Locate and identify every blood parasite.
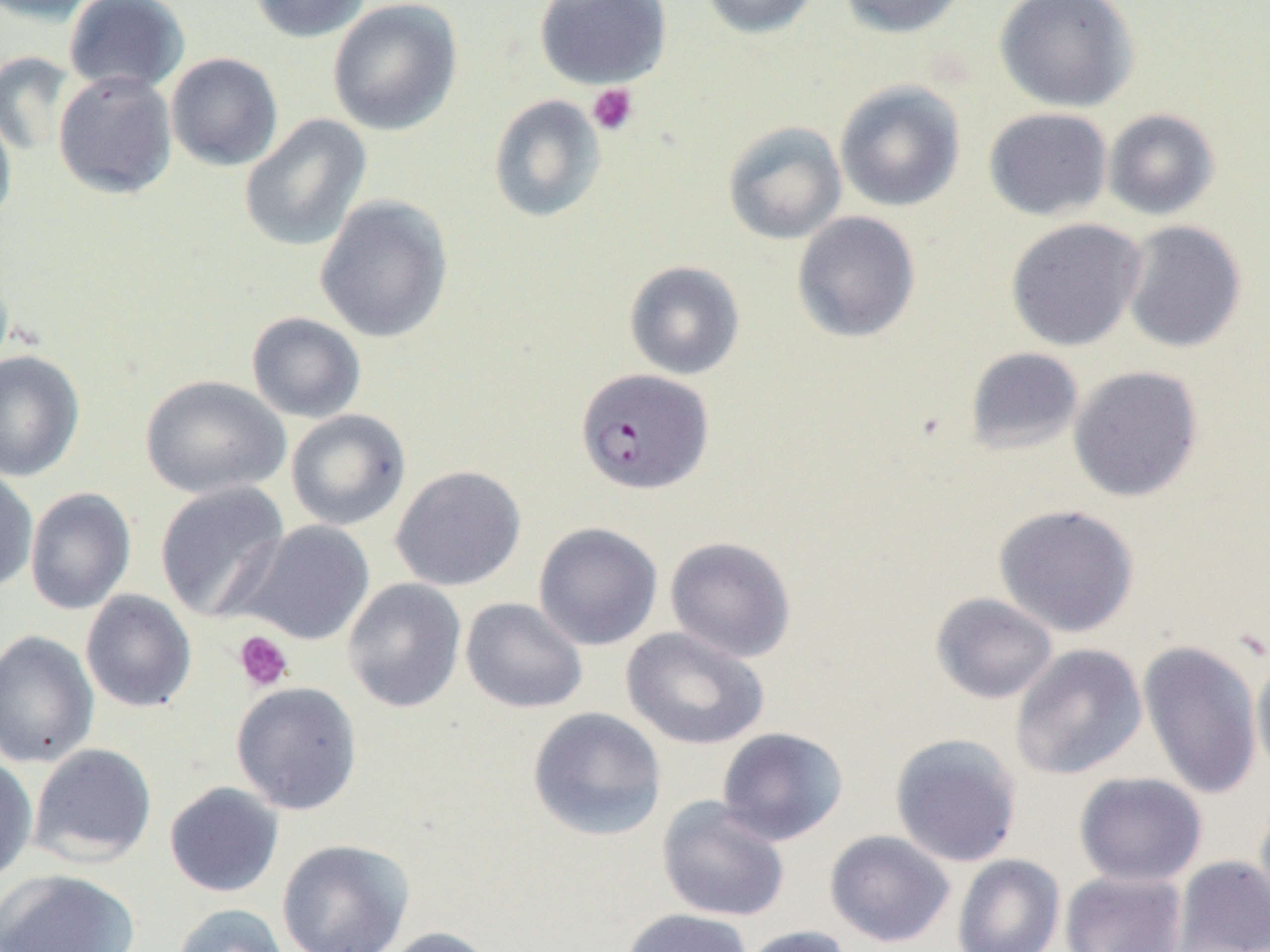

Approximate bounding boxes as [x1, y1, x2, y2] in pixels.
Plasmodium falciparum-infected red blood cells: [575, 368, 713, 495].
No Plasmodium ovale, Plasmodium malariae, Plasmodium vivax, Babesia divergens, or Trypanosoma brucei observed.

Uninfected red blood cell locations: [64, 0, 190, 94], [249, 0, 373, 43], [534, 0, 671, 89], [698, 0, 822, 39], [836, 0, 968, 38], [995, 0, 1140, 112], [0, 1, 102, 25], [327, 1, 463, 136], [0, 50, 75, 156], [166, 52, 283, 171], [53, 71, 177, 199], [834, 81, 965, 212], [488, 95, 606, 223], [0, 102, 17, 232], [983, 107, 1113, 221], [990, 108, 1116, 348], [1103, 108, 1221, 220], [239, 114, 372, 253], [722, 121, 847, 245], [314, 194, 454, 343], [792, 211, 921, 343], [1005, 218, 1145, 351], [1120, 220, 1247, 353], [624, 260, 745, 380], [246, 311, 366, 423], [965, 346, 1084, 456], [0, 350, 85, 482], [1068, 365, 1203, 502], [140, 374, 291, 499], [285, 409, 411, 531], [391, 464, 526, 592], [0, 467, 38, 593], [155, 481, 290, 622], [24, 487, 136, 615], [994, 503, 1139, 637], [237, 520, 374, 646], [533, 522, 663, 651], [665, 536, 796, 662], [342, 578, 467, 713], [80, 590, 197, 713], [930, 592, 1058, 704], [460, 597, 588, 714], [621, 626, 770, 750], [0, 630, 99, 768], [1137, 639, 1264, 800], [1010, 643, 1147, 780], [1251, 655, 1270, 782], [231, 681, 363, 815], [527, 706, 668, 842], [716, 727, 849, 845], [889, 733, 1023, 867], [28, 743, 157, 866], [0, 756, 37, 885], [1074, 772, 1207, 887], [164, 782, 284, 898], [656, 797, 790, 922], [1254, 800, 1270, 924], [825, 830, 956, 948], [276, 838, 415, 952], [952, 854, 1065, 952], [1171, 856, 1270, 952], [0, 869, 141, 952], [1059, 870, 1187, 952], [171, 903, 290, 952], [617, 908, 754, 952], [734, 925, 853, 952], [375, 926, 501, 952]. Platelet locations: [586, 83, 638, 136], [233, 630, 294, 692]. Slide-level diagnosis: Plasmodium falciparum. 1000x magnification. Single field of view. Image is 1270×952 pixels. Thin blood film. Optical microscopy.